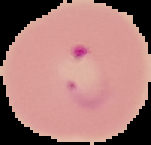
Summary:
  - Result: malaria parasites detected
  - Image type: cell region segmented out of the field of view; surrounding area masked to black
  - Image size: 151×145 pixels
  - Preparation: thin blood film